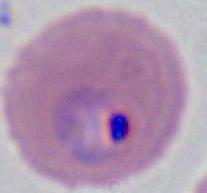

{
  "identification": "Plasmodium",
  "magnification": "400x or 1000x",
  "modality": "micrograph"
}